State which parasite is depicted.
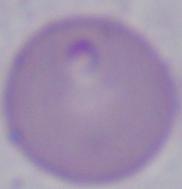

This is Babesia.

magnification = 1000x
modality = micrograph